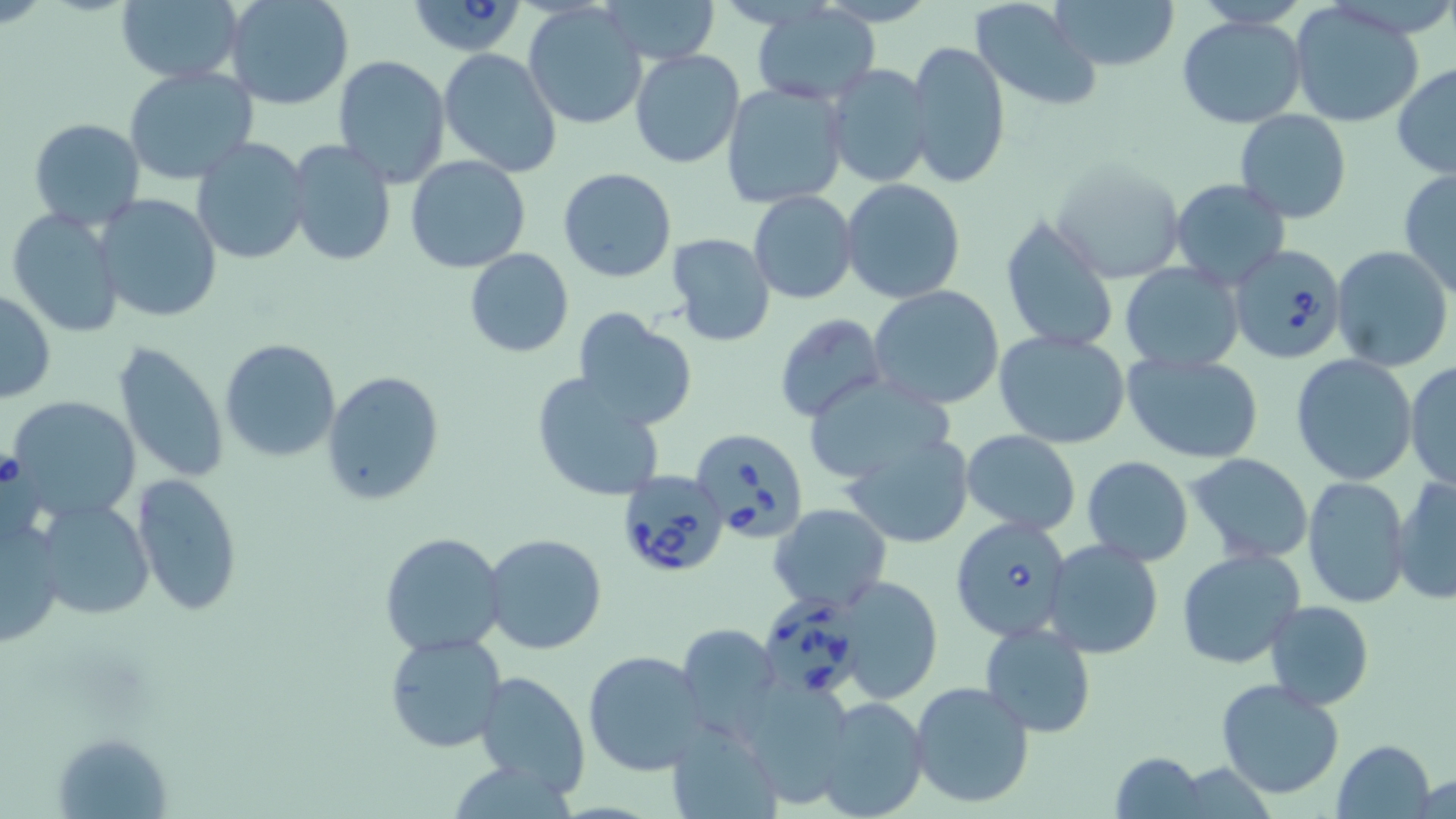

Babesia divergens-infected red blood cell locations = approximate bounding boxes as (x1,y1)-(x2,y2) corner pairs in pixels: (411,0)-(530,56), (1230,244)-(1348,365), (689,427)-(808,545), (614,469)-(730,579), (949,514)-(1071,643), (763,593)-(864,703)
slide-level diagnosis = Babesia divergens
preparation = thin blood smear
modality = light microscopy
stain = May-Grünwald-Giemsa
magnification = 1000x
field of view = one of a larger specimen
uninfected red blood cell locations = approximate bounding boxes as (x1,y1)-(x2,y2) corner pairs in pixels: (116,0)-(243,84), (224,0)-(354,110), (1053,0)-(1180,74), (970,1)-(1101,113), (602,2)-(722,64), (1290,3)-(1424,127), (523,4)-(648,130), (751,5)-(879,105), (1178,14)-(1306,129), (907,39)-(1010,190), (437,48)-(562,178), (629,49)-(744,168), (332,55)-(450,187), (824,63)-(934,188), (1392,63)-(1456,180), (123,65)-(258,185), (721,82)-(850,209), (1233,110)-(1354,224), (28,118)-(147,230), (191,138)-(310,265), (286,141)-(396,265), (405,156)-(532,274), (1052,159)-(1184,283), (557,166)-(678,283), (1397,170)-(1456,298), (1170,178)-(1291,289), (841,179)-(966,303), (749,190)-(858,304), (94,193)-(223,323), (6,208)-(126,338), (998,214)-(1121,355), (665,232)-(777,346), (1332,245)-(1453,372), (464,250)-(574,358), (1120,262)-(1245,372), (869,285)-(1005,410), (0,289)-(56,404), (573,311)-(697,430), (774,313)-(885,422), (994,331)-(1132,448), (219,338)-(341,462), (112,339)-(230,485), (1122,352)-(1264,462), (1290,355)-(1419,485), (1406,360)-(1455,490), (322,371)-(447,507), (531,372)-(668,502), (803,372)-(952,487), (9,396)-(142,523), (962,430)-(1082,536), (844,434)-(973,548), (1187,454)-(1312,563), (1082,455)-(1193,565), (132,472)-(243,615), (1302,475)-(1411,608), (1391,475)-(1456,604), (38,500)-(154,620), (770,503)-(892,613), (0,514)-(67,646), (379,532)-(507,656), (482,533)-(608,656), (1044,539)-(1164,659), (1175,548)-(1306,669), (833,575)-(943,705), (1265,599)-(1373,708), (674,621)-(782,739), (980,621)-(1097,739), (384,630)-(506,752), (582,650)-(706,776), (473,670)-(590,796), (1216,678)-(1347,801), (909,681)-(1035,808), (810,696)-(931,819), (666,721)-(781,818), (54,730)-(173,819), (1333,739)-(1436,819), (1110,752)-(1206,819), (1412,773)-(1455,818)
image size = 1456×819 pixels